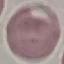
Malaria status: uninfected. Thin blood smear. Photographed with a smartphone camera at the microscope eyepiece. Giemsa stain. Automatically extracted cell patch, resized to 64 × 64 pixels.